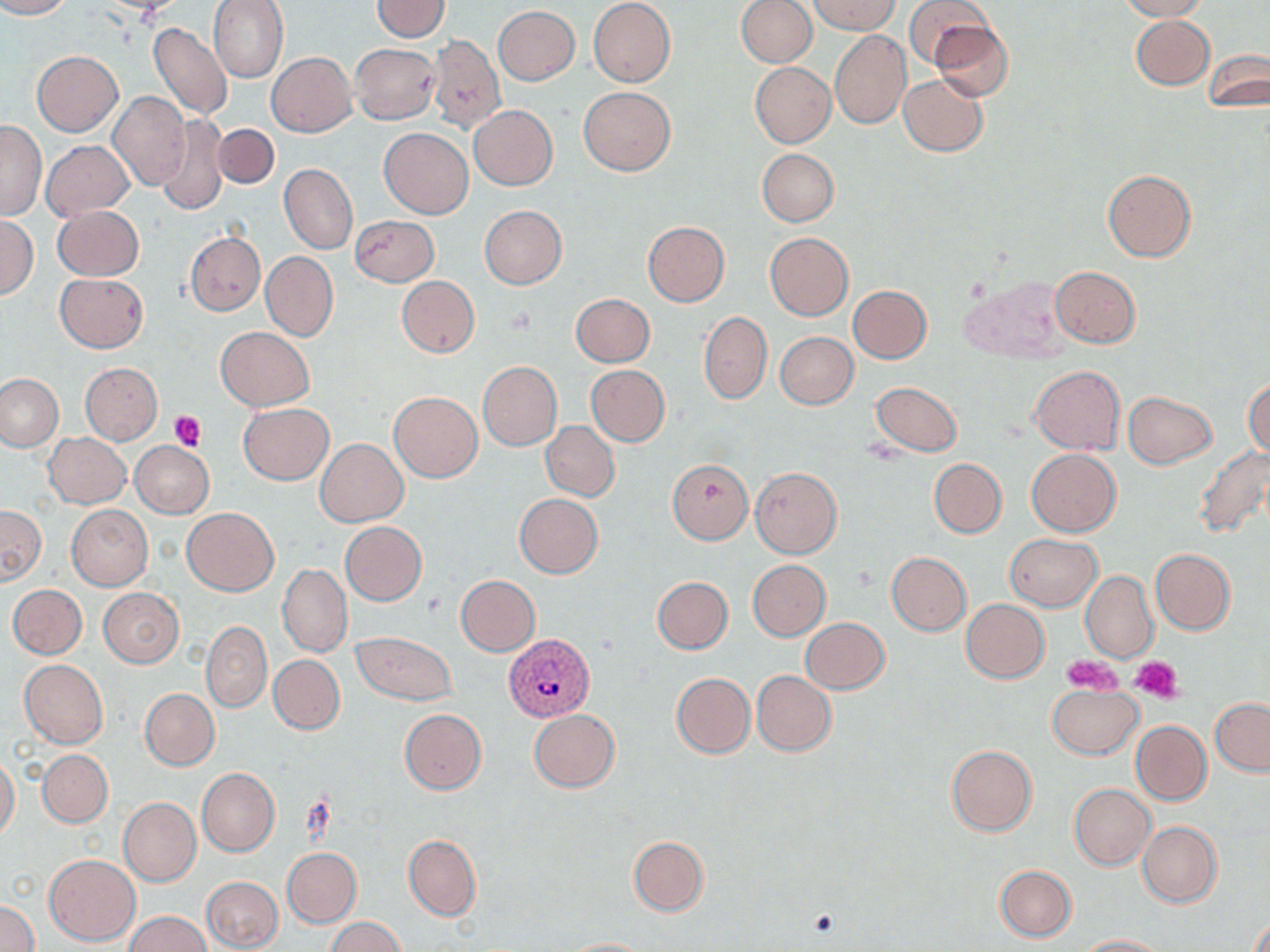

slide-level diagnosis = Plasmodium vivax
modality = light microscopy
Plasmodium vivax-infected red blood cell locations = approximate bounding boxes as (x1, y1, x2, y2) in pixels: (506, 634, 595, 721)
field of view = single
preparation = thin blood film
stain = May-Grünwald-Giemsa
uninfected red blood cell locations = approximate bounding boxes as (x1, y1, x2, y2) in pixels: (0, 0, 73, 19), (209, 0, 289, 83), (373, 0, 448, 41), (588, 0, 676, 88), (736, 0, 816, 67), (811, 0, 898, 34), (1117, 0, 1207, 21), (902, 1, 990, 70), (493, 6, 580, 85), (1131, 16, 1214, 90), (931, 19, 1013, 103), (148, 22, 233, 121), (830, 31, 910, 129), (428, 34, 505, 133), (349, 43, 441, 124), (1203, 49, 1268, 111), (32, 52, 122, 136), (266, 52, 356, 136), (750, 63, 836, 148), (898, 73, 988, 156), (580, 86, 676, 175), (107, 91, 190, 192), (469, 105, 558, 190), (157, 115, 229, 216), (1, 121, 45, 219), (212, 124, 279, 189), (379, 128, 473, 219), (42, 140, 133, 220), (757, 148, 838, 226), (280, 164, 357, 254), (1102, 169, 1196, 262), (54, 205, 143, 280), (479, 205, 568, 289), (351, 215, 439, 286), (0, 216, 38, 299), (642, 222, 730, 307), (186, 232, 264, 315), (765, 232, 853, 320), (260, 251, 337, 341), (1050, 266, 1141, 347), (54, 273, 147, 352), (396, 275, 480, 357), (961, 276, 1069, 361), (848, 285, 932, 363), (571, 293, 654, 367), (699, 312, 771, 404), (214, 327, 314, 410), (774, 331, 858, 409), (80, 362, 163, 444), (477, 362, 561, 450), (586, 365, 670, 446), (1028, 365, 1125, 454), (1, 372, 63, 450), (1244, 376, 1270, 459), (870, 382, 963, 456), (389, 391, 483, 482), (1123, 392, 1217, 468), (239, 403, 333, 484), (541, 422, 619, 501), (44, 433, 130, 508), (316, 438, 408, 526), (130, 441, 214, 518), (1194, 445, 1270, 539), (1027, 449, 1121, 536), (1019, 450, 1110, 612), (929, 458, 1006, 538), (667, 459, 752, 544), (751, 466, 842, 559), (515, 493, 603, 578), (0, 505, 45, 585), (67, 505, 152, 590), (181, 508, 279, 595), (340, 521, 427, 605), (1006, 534, 1102, 610), (1150, 549, 1236, 634), (887, 552, 971, 635), (748, 560, 830, 640), (277, 563, 351, 657), (1081, 569, 1159, 663), (454, 575, 540, 656), (653, 577, 732, 653), (8, 584, 87, 659), (98, 588, 183, 668), (961, 599, 1049, 682), (801, 618, 890, 694), (201, 622, 272, 712), (768, 627, 886, 732), (353, 632, 457, 705), (269, 655, 344, 734), (19, 659, 108, 748), (751, 671, 836, 756), (671, 672, 754, 757), (1047, 685, 1143, 759), (140, 688, 219, 770), (1210, 698, 1270, 775), (400, 709, 486, 794), (528, 710, 619, 793), (1131, 721, 1211, 805), (946, 745, 1037, 836), (38, 750, 112, 826), (0, 756, 20, 838), (197, 768, 279, 857), (1070, 784, 1155, 870), (119, 798, 201, 886), (1137, 821, 1222, 907), (403, 834, 481, 921), (628, 837, 709, 915), (282, 847, 362, 927), (43, 854, 140, 946), (995, 865, 1076, 942), (201, 876, 283, 951), (0, 900, 39, 952), (1247, 908, 1269, 952), (124, 911, 212, 952), (326, 916, 406, 951), (1075, 934, 1169, 951), (559, 937, 656, 952)
image size = 1270×952 pixels
magnification = 1000x
platelet locations = approximate bounding boxes as (x1, y1, x2, y2) in pixels: (505, 305, 539, 335), (170, 410, 205, 451), (422, 592, 445, 617), (1064, 654, 1122, 691), (1130, 655, 1184, 702), (806, 907, 841, 940)